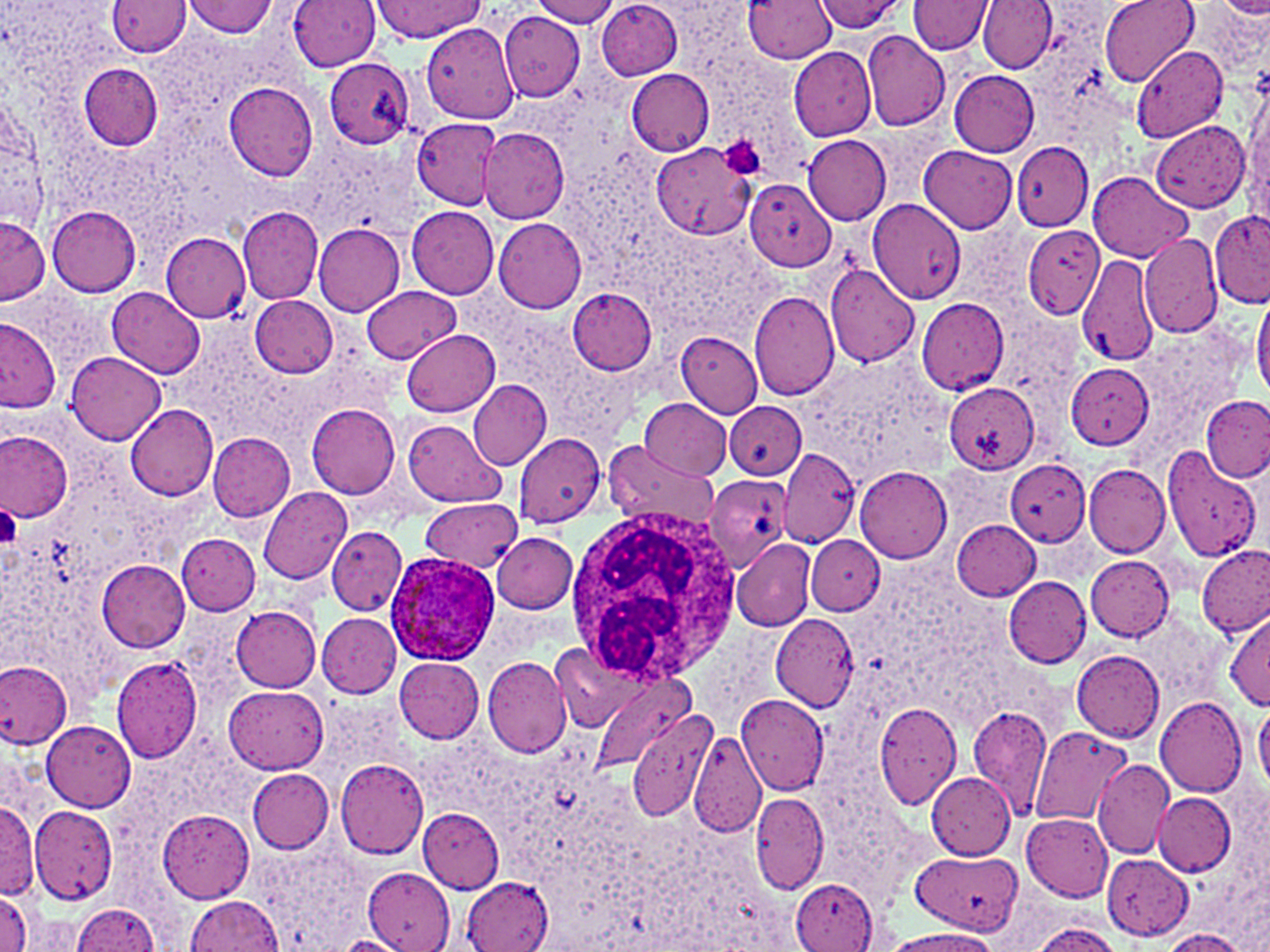
Summary:
  - Coordinate format: approximate bounding boxes as named x1/y1/x2/y2 corners in pixels
  - White blood cell locations: (x1=565, y1=510, x2=743, y2=681)
  - Platelet locations: (x1=722, y1=140, x2=766, y2=180), (x1=0, y1=505, x2=22, y2=550)
  - Plasmodium ovale-infected red blood cell locations: (x1=384, y1=552, x2=500, y2=667)
  - Uninfected red blood cell locations: (x1=288, y1=0, x2=384, y2=70), (x1=532, y1=0, x2=620, y2=27), (x1=744, y1=0, x2=837, y2=64), (x1=813, y1=0, x2=908, y2=32), (x1=979, y1=0, x2=1058, y2=73), (x1=1100, y1=0, x2=1198, y2=85), (x1=107, y1=1, x2=191, y2=55), (x1=184, y1=1, x2=278, y2=37), (x1=368, y1=1, x2=487, y2=42), (x1=596, y1=1, x2=683, y2=80), (x1=908, y1=1, x2=995, y2=54), (x1=500, y1=10, x2=586, y2=101), (x1=422, y1=24, x2=520, y2=124), (x1=861, y1=30, x2=950, y2=132), (x1=1131, y1=43, x2=1228, y2=143), (x1=788, y1=44, x2=877, y2=139), (x1=324, y1=58, x2=415, y2=147), (x1=77, y1=63, x2=163, y2=151), (x1=627, y1=69, x2=714, y2=157), (x1=949, y1=70, x2=1039, y2=157), (x1=1245, y1=71, x2=1270, y2=222), (x1=222, y1=82, x2=321, y2=180), (x1=3, y1=92, x2=41, y2=225), (x1=413, y1=118, x2=504, y2=209), (x1=1151, y1=121, x2=1250, y2=212), (x1=479, y1=129, x2=568, y2=224), (x1=802, y1=135, x2=891, y2=225), (x1=1010, y1=141, x2=1115, y2=230), (x1=651, y1=142, x2=757, y2=240), (x1=918, y1=146, x2=1018, y2=233), (x1=1087, y1=171, x2=1192, y2=262), (x1=744, y1=178, x2=837, y2=272), (x1=868, y1=198, x2=965, y2=304), (x1=45, y1=205, x2=140, y2=296), (x1=236, y1=205, x2=324, y2=305), (x1=406, y1=205, x2=499, y2=298), (x1=1209, y1=210, x2=1270, y2=310), (x1=494, y1=217, x2=587, y2=314), (x1=0, y1=219, x2=48, y2=303), (x1=313, y1=222, x2=404, y2=318), (x1=1022, y1=228, x2=1102, y2=319), (x1=160, y1=232, x2=252, y2=322), (x1=1138, y1=234, x2=1223, y2=339), (x1=1076, y1=253, x2=1162, y2=367), (x1=824, y1=265, x2=920, y2=367), (x1=107, y1=286, x2=205, y2=378), (x1=361, y1=286, x2=460, y2=364), (x1=566, y1=286, x2=657, y2=375), (x1=1251, y1=289, x2=1270, y2=400), (x1=749, y1=291, x2=841, y2=400), (x1=250, y1=295, x2=338, y2=377), (x1=915, y1=297, x2=1008, y2=394), (x1=1, y1=317, x2=61, y2=412), (x1=403, y1=329, x2=500, y2=417), (x1=676, y1=333, x2=763, y2=417), (x1=65, y1=352, x2=165, y2=445), (x1=1065, y1=362, x2=1154, y2=449), (x1=469, y1=378, x2=551, y2=470), (x1=944, y1=384, x2=1039, y2=474), (x1=1201, y1=395, x2=1270, y2=482), (x1=639, y1=398, x2=732, y2=480), (x1=725, y1=402, x2=806, y2=479), (x1=124, y1=403, x2=218, y2=502), (x1=308, y1=405, x2=402, y2=497), (x1=404, y1=421, x2=504, y2=508), (x1=0, y1=431, x2=72, y2=523), (x1=512, y1=432, x2=606, y2=527), (x1=209, y1=433, x2=294, y2=521), (x1=603, y1=440, x2=717, y2=528), (x1=769, y1=446, x2=862, y2=550), (x1=1162, y1=446, x2=1263, y2=562), (x1=998, y1=458, x2=1091, y2=555), (x1=1084, y1=464, x2=1171, y2=557), (x1=852, y1=465, x2=952, y2=563), (x1=703, y1=474, x2=791, y2=571), (x1=259, y1=486, x2=352, y2=585), (x1=420, y1=499, x2=522, y2=570), (x1=951, y1=519, x2=1041, y2=600), (x1=327, y1=527, x2=409, y2=615), (x1=176, y1=533, x2=260, y2=613), (x1=491, y1=533, x2=578, y2=613), (x1=730, y1=537, x2=817, y2=631), (x1=806, y1=537, x2=882, y2=614), (x1=1198, y1=545, x2=1270, y2=637), (x1=1085, y1=555, x2=1175, y2=640), (x1=96, y1=559, x2=191, y2=653), (x1=1003, y1=576, x2=1093, y2=667), (x1=230, y1=604, x2=321, y2=693), (x1=1224, y1=609, x2=1269, y2=709), (x1=317, y1=613, x2=402, y2=698), (x1=769, y1=614, x2=859, y2=712), (x1=551, y1=641, x2=648, y2=733), (x1=1072, y1=649, x2=1164, y2=739), (x1=111, y1=655, x2=203, y2=764), (x1=482, y1=657, x2=573, y2=757), (x1=394, y1=658, x2=483, y2=741), (x1=0, y1=661, x2=73, y2=747), (x1=593, y1=675, x2=695, y2=770), (x1=224, y1=686, x2=328, y2=774), (x1=734, y1=692, x2=829, y2=794), (x1=1155, y1=695, x2=1247, y2=797), (x1=873, y1=700, x2=963, y2=812), (x1=1254, y1=702, x2=1270, y2=794), (x1=968, y1=705, x2=1053, y2=817), (x1=628, y1=711, x2=718, y2=824), (x1=40, y1=720, x2=135, y2=810), (x1=1027, y1=725, x2=1133, y2=826), (x1=688, y1=731, x2=765, y2=837), (x1=335, y1=758, x2=429, y2=860), (x1=1092, y1=758, x2=1174, y2=857), (x1=247, y1=769, x2=334, y2=853), (x1=925, y1=772, x2=1017, y2=860), (x1=751, y1=792, x2=829, y2=893), (x1=1153, y1=792, x2=1237, y2=876), (x1=0, y1=799, x2=39, y2=899), (x1=30, y1=805, x2=117, y2=905), (x1=417, y1=807, x2=505, y2=894), (x1=156, y1=810, x2=255, y2=903), (x1=1020, y1=814, x2=1114, y2=899), (x1=251, y1=841, x2=374, y2=951), (x1=908, y1=854, x2=1024, y2=935), (x1=1101, y1=854, x2=1194, y2=939), (x1=363, y1=867, x2=455, y2=951), (x1=791, y1=878, x2=877, y2=950), (x1=460, y1=879, x2=551, y2=951), (x1=0, y1=891, x2=34, y2=951), (x1=182, y1=896, x2=285, y2=951), (x1=70, y1=904, x2=161, y2=951), (x1=1025, y1=921, x2=1123, y2=951), (x1=886, y1=928, x2=1002, y2=952), (x1=1157, y1=929, x2=1252, y2=951)
  - Slide-level diagnosis: Plasmodium ovale
  - Stain: May-Grünwald-Giemsa
  - Image size: 1270×952 pixels
  - Preparation: thin blood film
  - Modality: light microscopy
  - Magnification: 1000x
  - Field of view: single